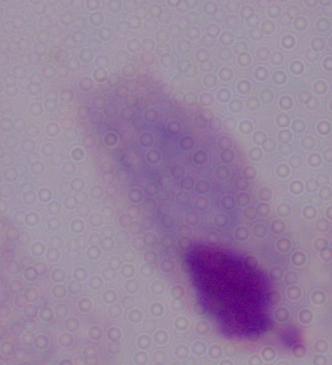

identification = trichomonad
modality = micrograph
magnification = 1000x